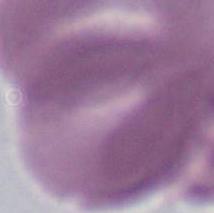

modality = micrograph
magnification = 1000x
identification = erythrocyte